Assess this cell for malaria.
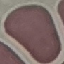

It is uninfected.

Thin blood film. Cell patch, automatically extracted from a larger field of view and resized to 64 × 64 pixels. Giemsa-stained preparation. Photographed with a smartphone camera at the microscope eyepiece.